Classify this cell by malaria status.
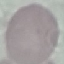
Uninfected.

Giemsa stain. Acquired by smartphone through the microscope eyepiece. Cell patch, automatically extracted from a larger field of view and resized to 64 × 64 pixels. Thin smear of blood.